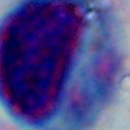
magnification: 1000x
modality: photomicrograph
identification: white blood cell